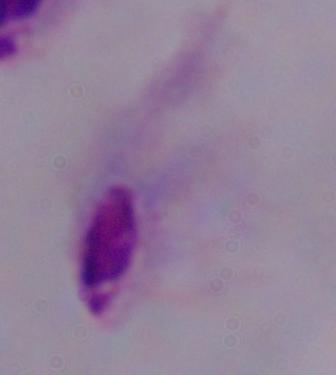 Photomicrograph. Captured at 1000x magnification. A trichomonad is seen.